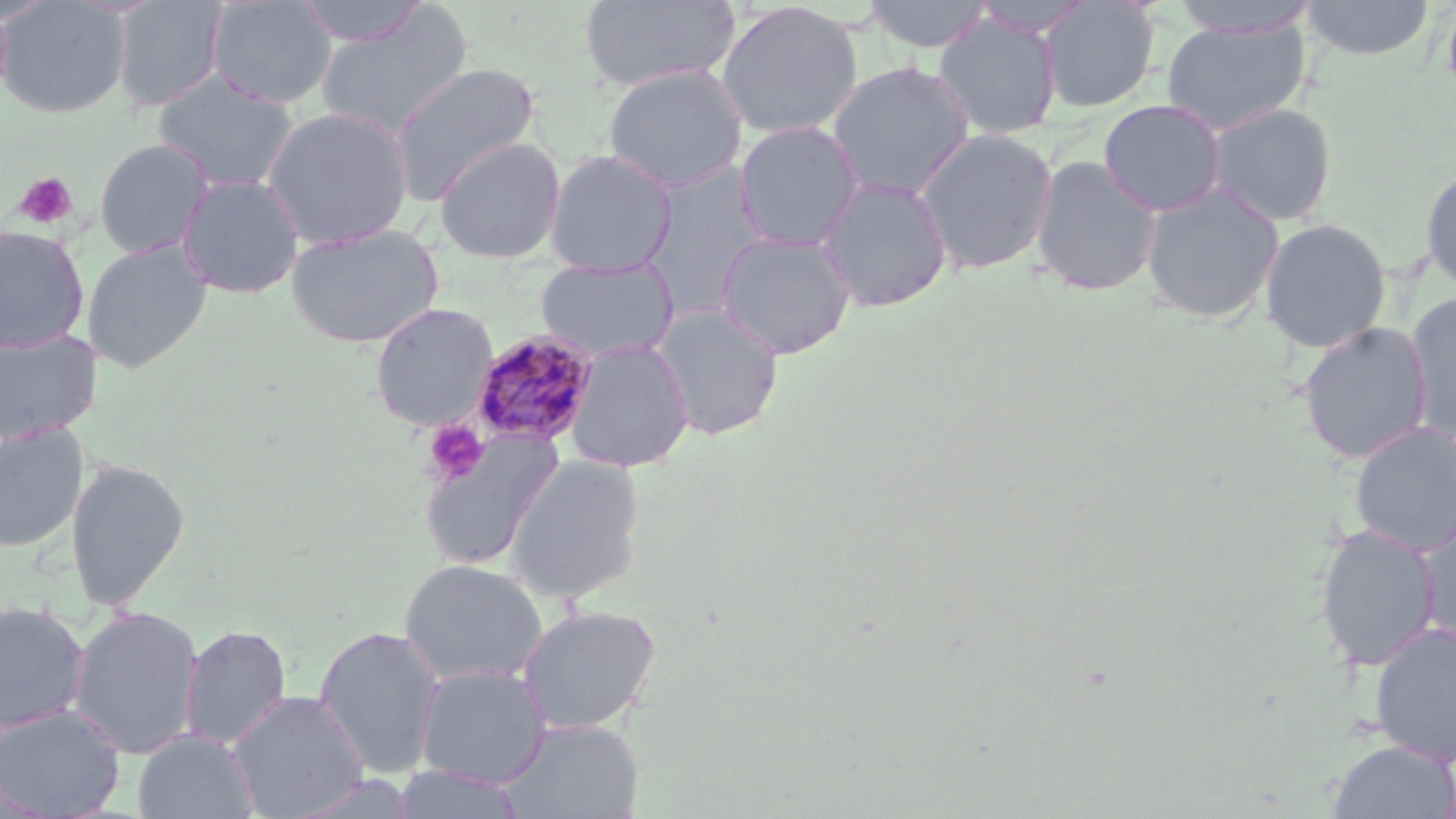

slide-level diagnosis = Plasmodium malariae
uninfected red blood cell locations = approximate bounding boxes as (x1, y1, x2, y2) in pixels: (0, 0, 132, 118), (112, 0, 229, 112), (206, 0, 337, 109), (292, 0, 430, 47), (579, 0, 740, 93), (861, 0, 995, 53), (970, 0, 1091, 38), (1037, 0, 1160, 113), (1301, 0, 1436, 61), (1441, 0, 1456, 112), (715, 1, 864, 140), (1168, 1, 1322, 38), (0, 3, 14, 107), (315, 5, 474, 141), (933, 12, 1063, 140), (1160, 18, 1312, 136), (826, 61, 974, 201), (388, 62, 541, 202), (603, 64, 748, 193), (153, 72, 299, 193), (1098, 98, 1227, 216), (1203, 101, 1338, 226), (261, 105, 414, 250), (733, 121, 864, 252), (914, 127, 1058, 276), (434, 136, 566, 264), (93, 138, 216, 259), (544, 149, 677, 276), (1030, 154, 1162, 296), (638, 163, 770, 319), (1420, 164, 1456, 294), (176, 173, 305, 299), (815, 175, 952, 313), (1140, 182, 1285, 325), (1258, 218, 1393, 354), (285, 223, 444, 348), (0, 225, 90, 352), (715, 229, 856, 360), (81, 240, 213, 372), (535, 256, 679, 363), (1404, 290, 1456, 442), (370, 302, 499, 431), (650, 303, 785, 440), (1297, 321, 1434, 465), (0, 328, 100, 444), (564, 338, 694, 473), (1349, 421, 1456, 556), (1, 423, 88, 552), (417, 431, 564, 570), (502, 453, 646, 605), (65, 457, 190, 611), (1416, 514, 1456, 651), (1313, 523, 1443, 671), (398, 559, 548, 687), (0, 601, 91, 734), (516, 603, 662, 736), (68, 605, 205, 761), (1368, 621, 1456, 766), (179, 624, 293, 750), (314, 625, 446, 779), (414, 663, 552, 788), (228, 689, 370, 819), (0, 703, 126, 818), (495, 717, 645, 819), (132, 729, 258, 819), (1326, 739, 1456, 819), (390, 764, 524, 819)
modality = optical microscopy
platelet locations = approximate bounding boxes as (x1, y1, x2, y2) in pixels: (14, 172, 78, 230), (422, 419, 490, 487)
stain = May-Grünwald-Giemsa
preparation = thin blood smear
field of view = one of a larger specimen
Plasmodium malariae-infected red blood cell locations = approximate bounding boxes as (x1, y1, x2, y2) in pixels: (469, 329, 599, 448)
magnification = 1000x
image size = 1456×819 pixels